Identify the blood parasite species.
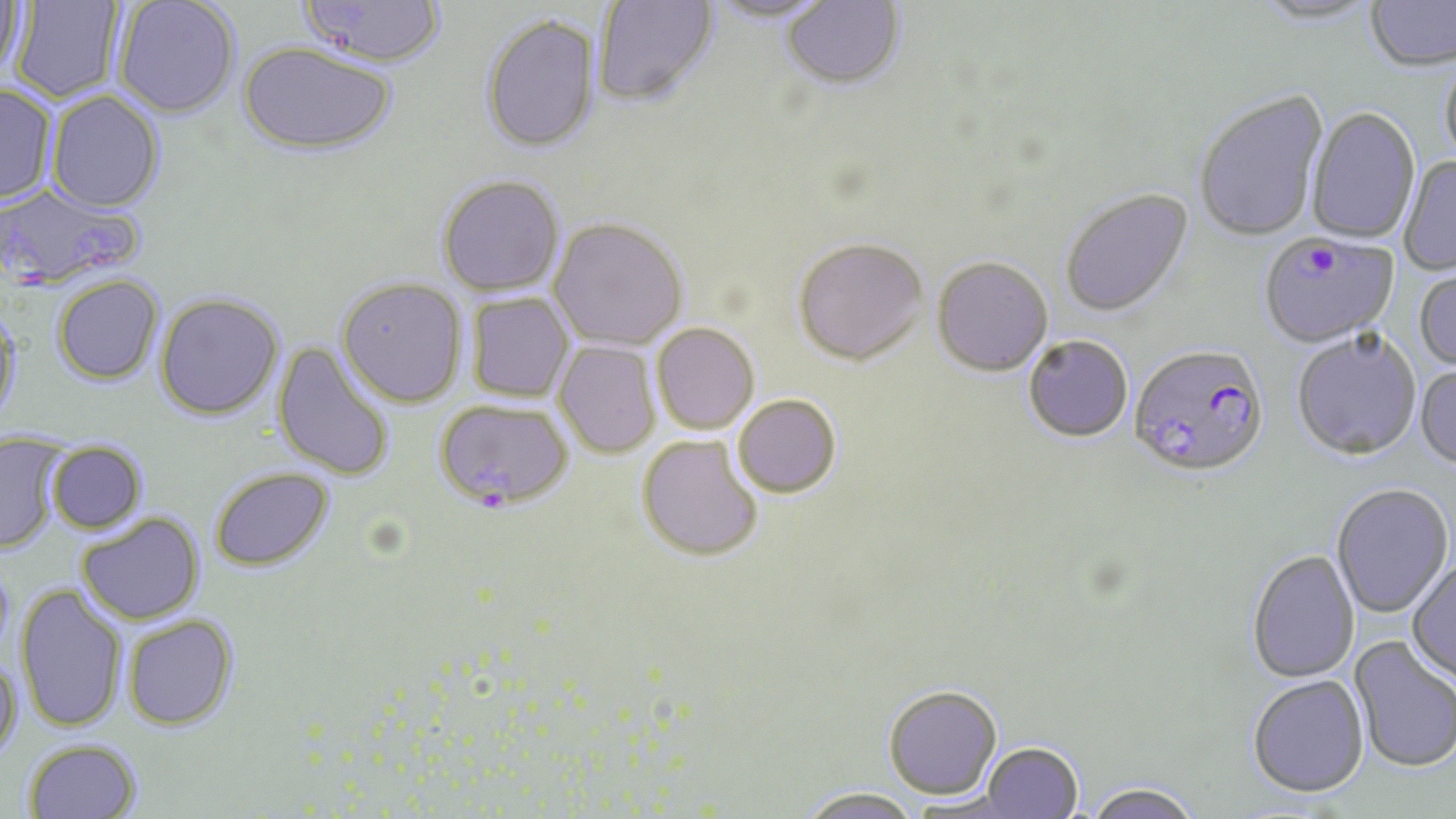
Plasmodium falciparum.

{
  "field_of_view": "single",
  "uninfected_red_blood_cell_locations": "approximate bounding boxes as (x1, y1, x2, y2) in pixels: (0, 0, 27, 79), (9, 0, 125, 104), (114, 0, 240, 119), (592, 0, 720, 109), (706, 0, 835, 25), (1251, 0, 1381, 26), (1365, 0, 1456, 73), (298, 1, 448, 70), (781, 1, 906, 92), (480, 14, 600, 154), (238, 42, 396, 157), (1440, 54, 1456, 173), (0, 84, 57, 206), (46, 91, 164, 213), (1194, 91, 1328, 244), (1306, 107, 1421, 246), (1399, 156, 1456, 277), (437, 175, 566, 298), (1060, 189, 1195, 319), (548, 219, 688, 352), (792, 240, 929, 367), (932, 258, 1053, 378), (1414, 266, 1456, 373), (52, 275, 164, 385), (336, 277, 468, 407), (155, 292, 284, 421), (466, 292, 575, 403), (0, 303, 24, 434), (651, 324, 759, 435), (1292, 332, 1422, 462), (1023, 336, 1133, 444), (272, 340, 397, 482), (553, 340, 661, 460), (1415, 366, 1456, 473), (733, 396, 842, 500), (636, 436, 763, 564), (46, 441, 148, 534), (0, 443, 63, 554), (210, 467, 335, 572), (1332, 485, 1454, 617), (77, 513, 204, 625), (1247, 550, 1359, 684), (1407, 558, 1456, 685), (15, 584, 127, 733), (123, 614, 239, 731), (1348, 636, 1455, 774), (0, 654, 23, 762), (1246, 676, 1369, 801), (885, 688, 1002, 802), (23, 738, 142, 819), (981, 744, 1083, 818), (1082, 785, 1203, 819), (796, 790, 923, 819)",
  "image_size": "1456×819 pixels",
  "magnification": "1000x",
  "modality": "light microscopy",
  "stain": "May-Grünwald-Giemsa",
  "preparation": "thin blood film",
  "plasmodium_falciparum_infected_red_blood_cell_locations": "approximate bounding boxes as (x1, y1, x2, y2) in pixels: (0, 183, 146, 291), (1259, 234, 1399, 350), (1129, 346, 1269, 481), (435, 400, 573, 511)"
}